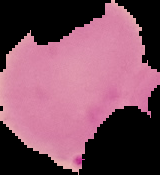

Image is 160×175 pixels. Cell region segmented out of the field of view; the surrounding area is masked to black. Result: malaria parasites detected. From a thin blood film.